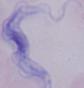
magnification = 1000x
identification = trypanosome
modality = micrograph